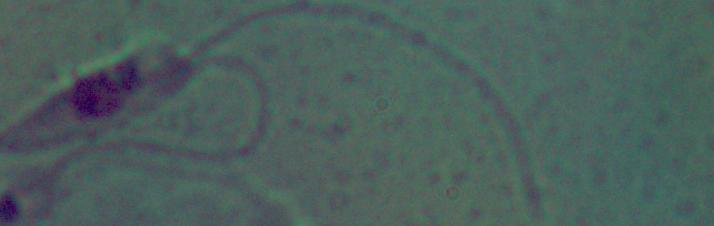
Summary:
  - Magnification: 1000x
  - Modality: photomicrograph
  - Identification: Leishmania